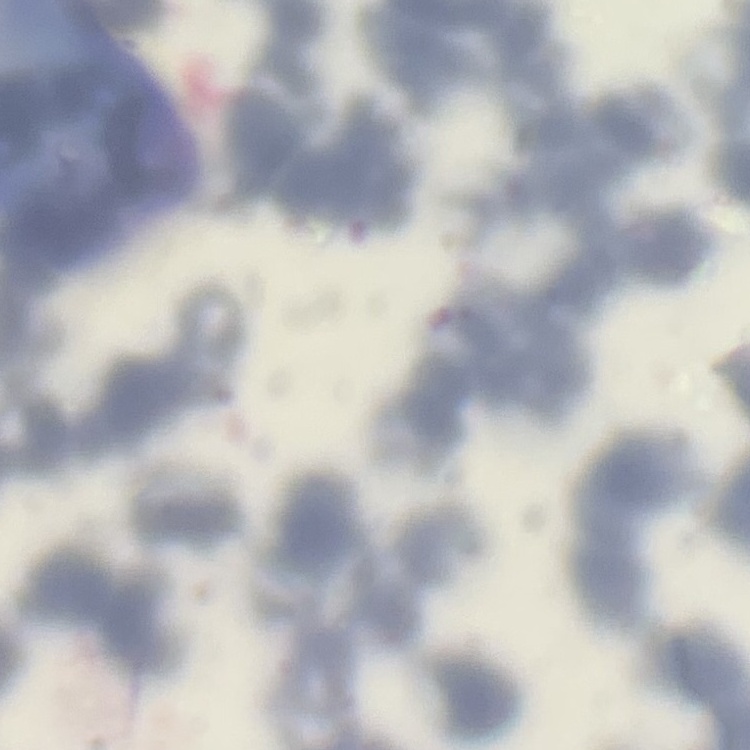
The red blood cells show rouleaux formation. Stained with either Field's or Giemsa. One tile cut from a larger photomicrograph. Thin peripheral smear.